Identify the blood parasite species.
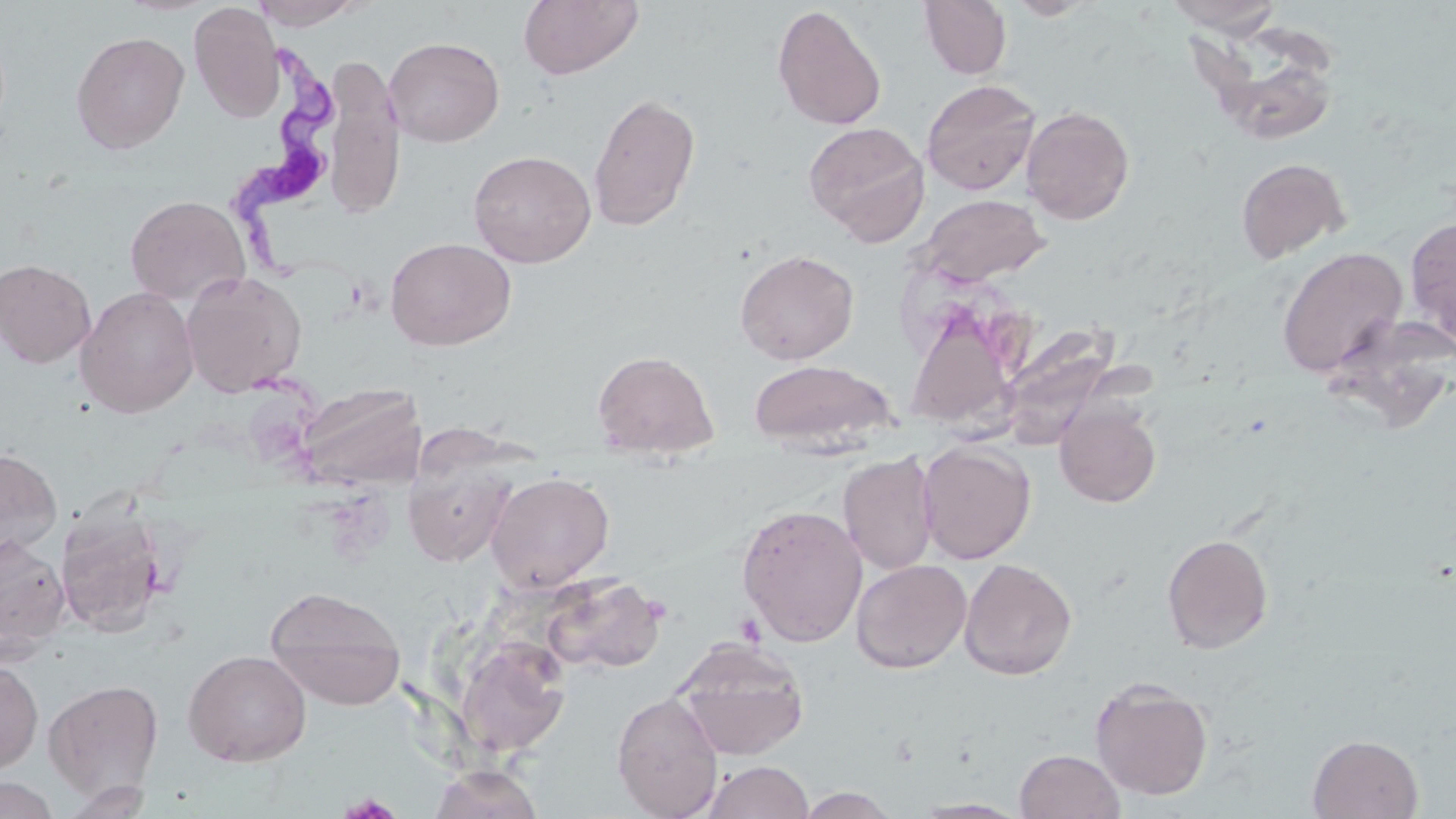
Trypanosoma brucei.

Summary:
  - Coordinate format: approximate bounding boxes as (x1, y1, x2, y2) in pixels
  - Platelet locations: (333, 793, 405, 818)
  - Trypanosoma brucei locations: (231, 38, 370, 309)
  - Uninfected red blood cell locations: (249, 0, 368, 29), (518, 0, 643, 81), (919, 0, 1012, 79), (1006, 0, 1101, 20), (1162, 0, 1285, 36), (187, 2, 285, 123), (771, 5, 887, 131), (71, 31, 190, 154), (1189, 33, 1335, 136), (383, 36, 505, 147), (921, 79, 1040, 195), (588, 91, 701, 232), (1022, 105, 1135, 225), (804, 121, 929, 245), (468, 150, 596, 268), (1236, 157, 1350, 263), (125, 194, 251, 306), (918, 194, 1049, 287), (1404, 216, 1456, 346), (385, 237, 517, 352), (1276, 246, 1408, 379), (734, 249, 859, 364), (0, 258, 96, 368), (180, 270, 307, 398), (76, 286, 199, 418), (905, 298, 1023, 446), (1000, 322, 1119, 448), (591, 348, 720, 460), (748, 358, 897, 453), (296, 384, 423, 489), (1055, 401, 1161, 508), (917, 441, 1036, 564), (0, 447, 63, 559), (839, 451, 939, 575), (404, 459, 515, 567), (486, 471, 615, 593), (736, 503, 868, 648), (55, 505, 167, 637), (0, 532, 69, 660), (1162, 533, 1274, 654), (959, 557, 1077, 680), (851, 559, 972, 674), (543, 573, 666, 674), (264, 585, 406, 710), (671, 637, 809, 760), (454, 639, 570, 756), (183, 649, 311, 767), (0, 659, 43, 773), (1089, 677, 1214, 800), (43, 678, 165, 800), (611, 691, 724, 819), (1307, 733, 1424, 818), (1014, 748, 1125, 819), (702, 759, 815, 819), (429, 764, 545, 819), (0, 776, 60, 819), (794, 786, 902, 818), (911, 798, 1030, 817)
  - Field of view: single
  - Image size: 1456×819 pixels
  - Magnification: 1000x
  - Stain: May-Grünwald-Giemsa
  - Modality: optical microscopy
  - Preparation: thin blood smear